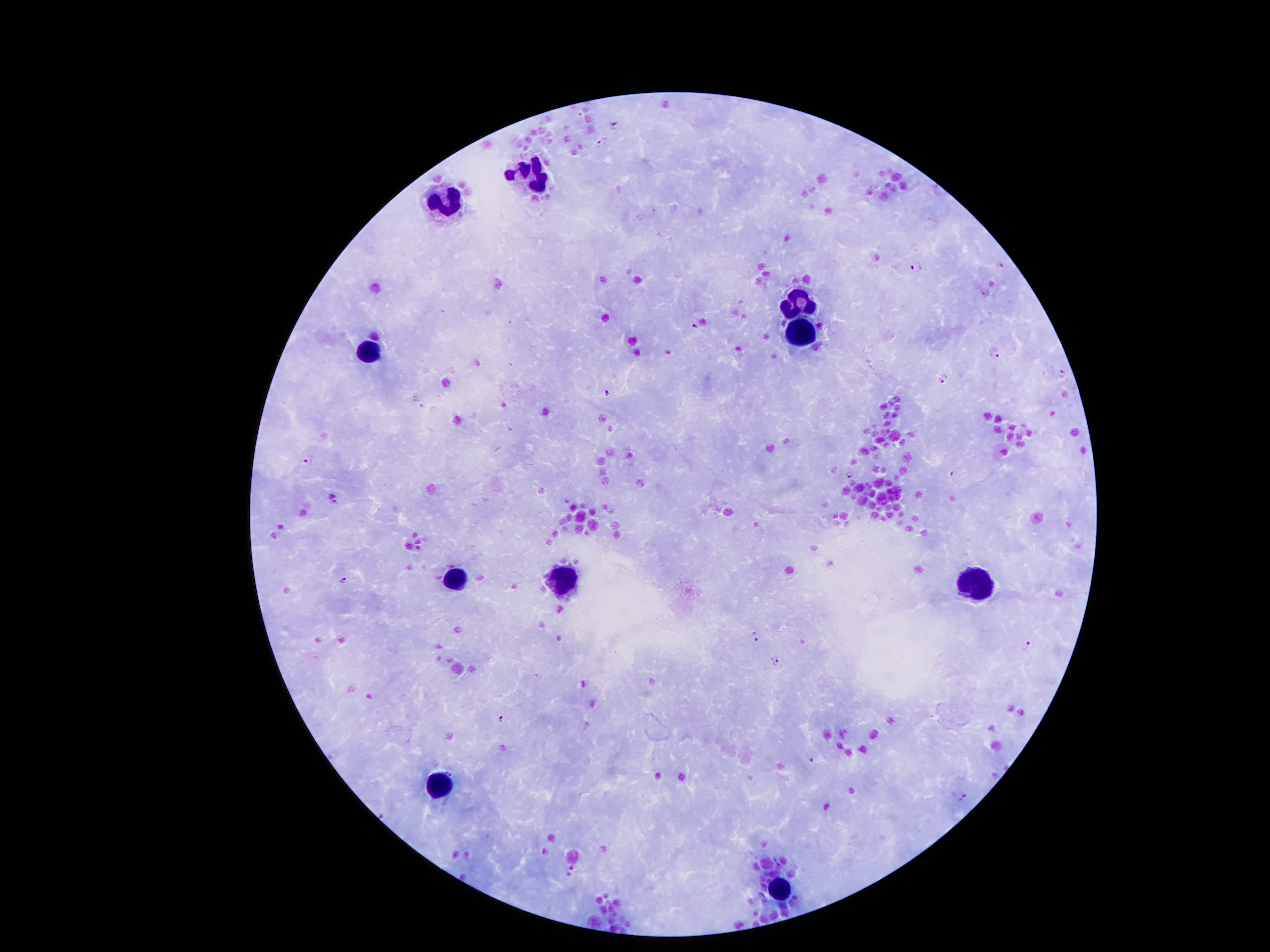

coordinate format = approximate centers as [x, y] in pixels
leukocyte locations = [539, 178], [448, 201], [805, 303], [796, 335], [364, 351], [453, 580], [564, 580], [970, 585]
malaria parasite locations = [616, 123], [600, 141], [916, 266], [693, 327], [995, 355], [1063, 370], [943, 377], [604, 392], [309, 459], [954, 474], [849, 475], [335, 502], [344, 581], [755, 637], [1025, 645], [774, 661], [501, 719], [810, 759], [450, 773], [965, 798]
capture = smartphone through the microscope eyepiece
image size = 1270×952 pixels
stain = Giemsa
field of view = one from this slide
patient malaria status = infected with Plasmodium falciparum
preparation = thick blood smear
magnification = 100x